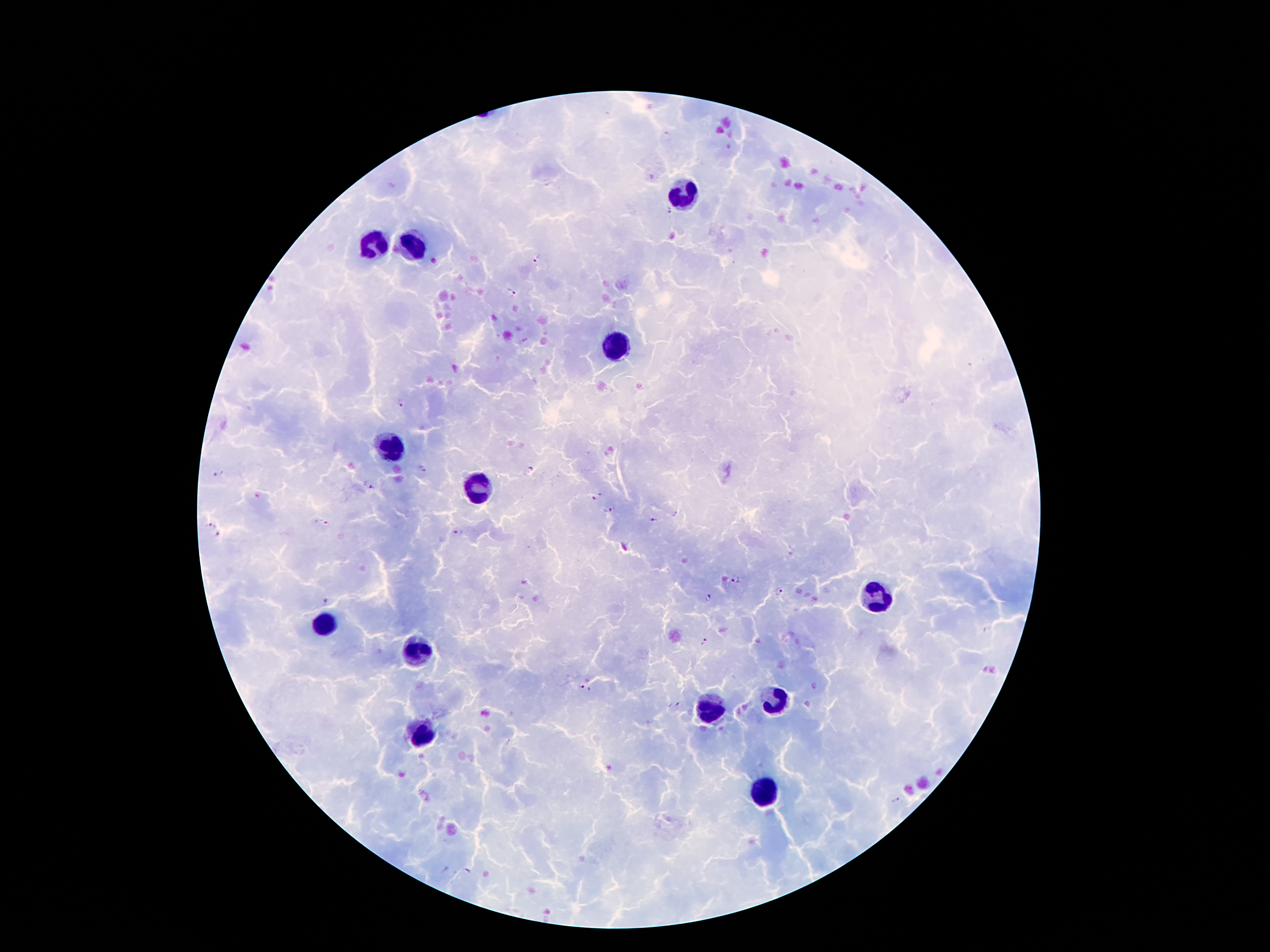

coordinate format = approximate centers as [x, y] in pixels
leukocyte locations = [684, 194], [376, 245], [410, 246], [616, 345], [392, 446], [475, 487], [877, 601], [326, 622], [414, 653], [774, 703], [710, 711], [420, 736], [763, 790]
malaria parasite locations = [665, 137], [668, 212], [538, 258], [511, 290], [402, 402], [421, 468], [530, 469], [219, 474], [372, 488], [594, 499], [611, 510], [653, 519], [210, 523], [322, 523], [457, 532], [216, 535], [734, 579], [777, 593], [707, 598], [325, 601], [704, 642], [814, 686], [584, 688], [677, 704], [898, 800], [467, 871]
magnification = 100x
capture = smartphone camera through the microscope eyepiece
preparation = thick blood smear
stain = Giemsa
field of view = single
patient malaria status = infected with Plasmodium falciparum
image size = 1270×952 pixels